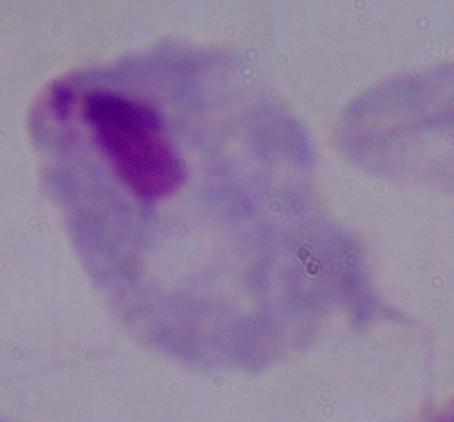

A trichomonad is shown. 1000x magnification. Micrograph.